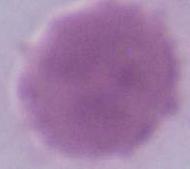

{
  "modality": "photomicrograph",
  "magnification": "1000x",
  "identification": "erythrocyte"
}